Classify this cell by malaria status.
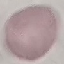
Uninfected.

Giemsa-stained preparation. Photographed with a smartphone camera at the microscope eyepiece. Automatically extracted cell patch, resized to 64 × 64 pixels. Thin blood film.